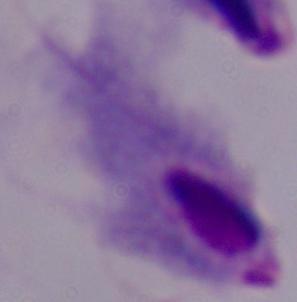
Summary:
  - Modality: photomicrograph
  - Magnification: 1000x
  - Identification: trichomonad